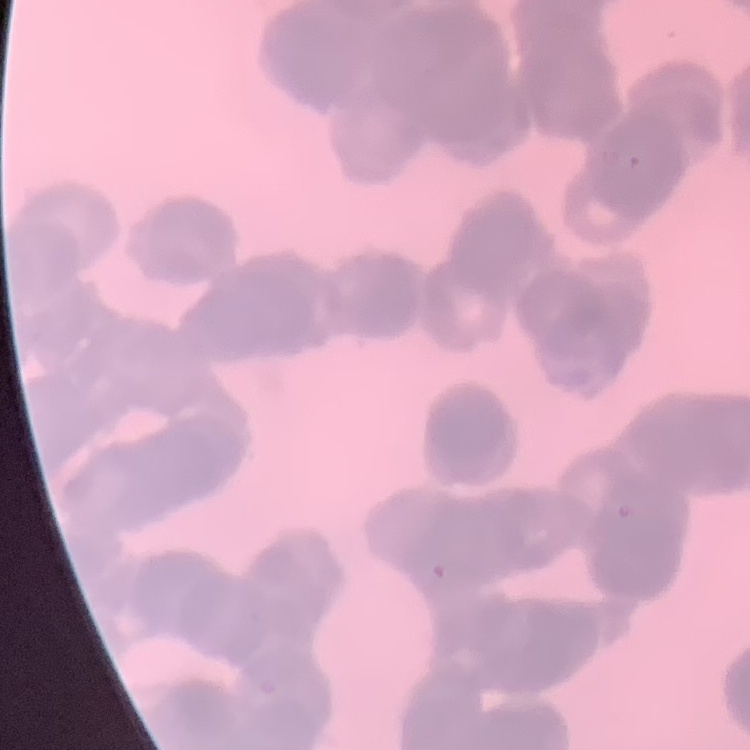

Summary:
  - Red blood cell morphology: rouleaux formation
  - Stain: Field's or Giemsa
  - Image type: square crop of a larger photomicrograph
  - Preparation: thin blood smear